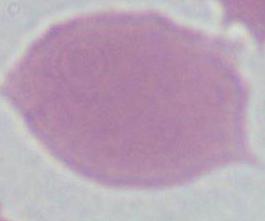

A red blood cell is seen. Micrograph. Captured at 1000x magnification.